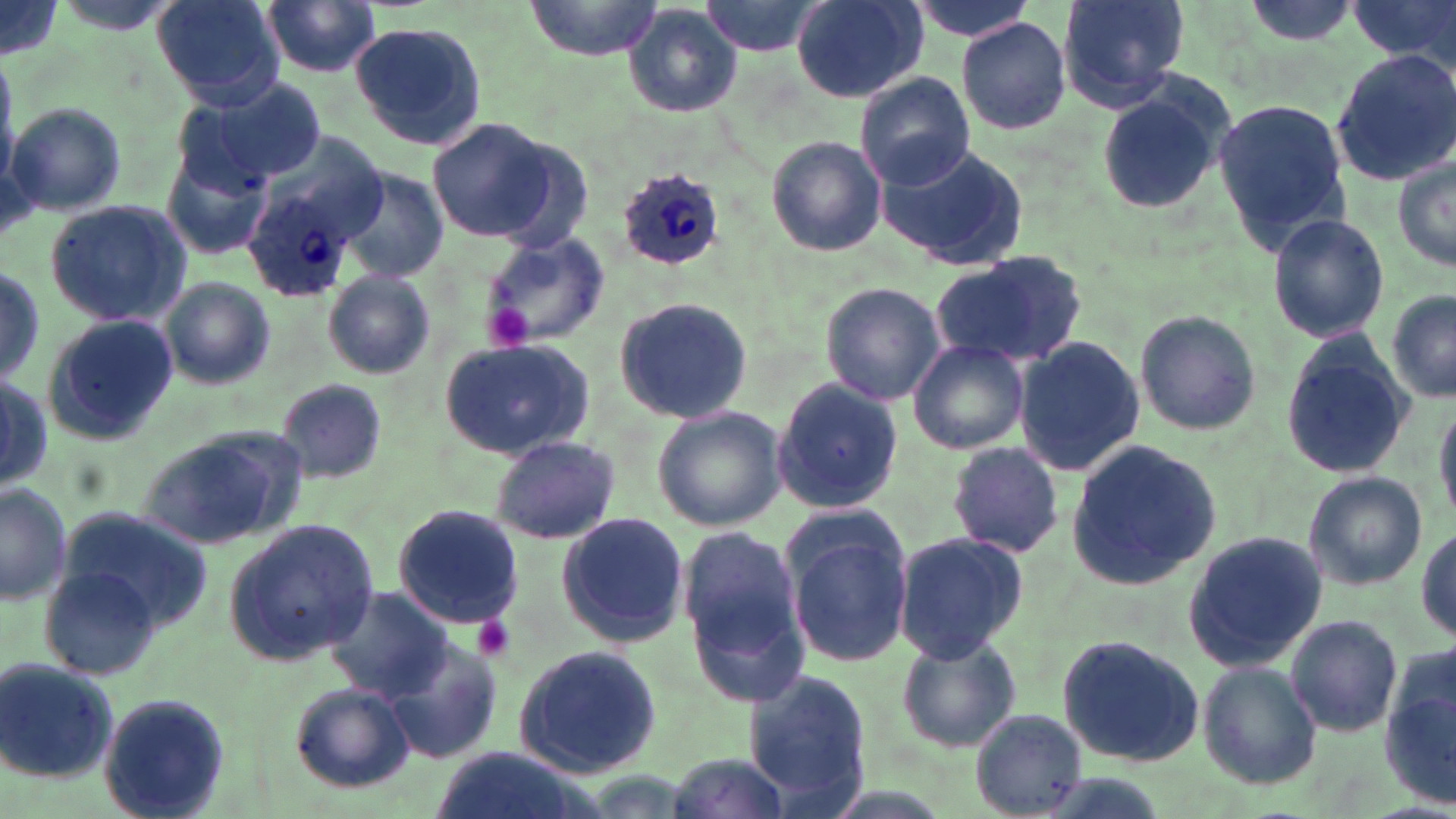

{
  "slide_level_diagnosis": "Plasmodium ovale",
  "magnification": "1000x",
  "stain": "May-Grünwald-Giemsa",
  "field_of_view": "single",
  "preparation": "thin blood smear",
  "modality": "optical microscopy",
  "image_size": "1456×819 pixels",
  "uninfected_red_blood_cell_locations": "approximate bounding boxes as named x1/y1/x2/y2 corners in pixels: (x1=152, y1=0, x2=284, y2=108), (x1=520, y1=0, x2=665, y2=60), (x1=700, y1=0, x2=829, y2=57), (x1=791, y1=0, x2=927, y2=102), (x1=902, y1=0, x2=1039, y2=44), (x1=1057, y1=0, x2=1191, y2=109), (x1=1236, y1=0, x2=1363, y2=48), (x1=1348, y1=0, x2=1456, y2=68), (x1=260, y1=1, x2=381, y2=79), (x1=0, y1=2, x2=61, y2=59), (x1=624, y1=6, x2=741, y2=117), (x1=956, y1=17, x2=1071, y2=134), (x1=349, y1=20, x2=487, y2=150), (x1=1329, y1=49, x2=1456, y2=184), (x1=855, y1=74, x2=977, y2=191), (x1=207, y1=77, x2=329, y2=186), (x1=1095, y1=86, x2=1227, y2=216), (x1=1214, y1=97, x2=1350, y2=255), (x1=8, y1=102, x2=127, y2=218), (x1=429, y1=118, x2=555, y2=241), (x1=486, y1=135, x2=597, y2=250), (x1=766, y1=135, x2=887, y2=256), (x1=877, y1=144, x2=1029, y2=269), (x1=159, y1=146, x2=275, y2=264), (x1=1391, y1=157, x2=1456, y2=274), (x1=336, y1=169, x2=449, y2=281), (x1=42, y1=198, x2=191, y2=326), (x1=1266, y1=212, x2=1389, y2=344), (x1=479, y1=229, x2=612, y2=349), (x1=933, y1=254, x2=1088, y2=369), (x1=0, y1=262, x2=46, y2=390), (x1=321, y1=269, x2=436, y2=379), (x1=159, y1=278, x2=276, y2=390), (x1=819, y1=280, x2=946, y2=405), (x1=1386, y1=290, x2=1456, y2=403), (x1=612, y1=297, x2=756, y2=427), (x1=1132, y1=309, x2=1265, y2=437), (x1=37, y1=315, x2=177, y2=444), (x1=441, y1=335, x2=593, y2=457), (x1=1016, y1=336, x2=1144, y2=475), (x1=1279, y1=336, x2=1418, y2=481), (x1=907, y1=339, x2=1029, y2=455), (x1=0, y1=371, x2=51, y2=494), (x1=769, y1=377, x2=904, y2=514), (x1=273, y1=379, x2=387, y2=484), (x1=1433, y1=397, x2=1455, y2=525), (x1=651, y1=406, x2=783, y2=532), (x1=138, y1=424, x2=304, y2=549), (x1=488, y1=435, x2=622, y2=546), (x1=1066, y1=441, x2=1223, y2=588), (x1=947, y1=442, x2=1062, y2=558), (x1=1304, y1=471, x2=1428, y2=590), (x1=0, y1=482, x2=73, y2=606), (x1=392, y1=504, x2=522, y2=629), (x1=55, y1=508, x2=214, y2=629), (x1=555, y1=512, x2=691, y2=649), (x1=225, y1=516, x2=378, y2=665), (x1=679, y1=521, x2=811, y2=698), (x1=1414, y1=523, x2=1454, y2=646), (x1=785, y1=526, x2=913, y2=668), (x1=891, y1=531, x2=1028, y2=663), (x1=1181, y1=532, x2=1328, y2=670), (x1=42, y1=567, x2=165, y2=681), (x1=326, y1=587, x2=454, y2=700), (x1=1286, y1=614, x2=1403, y2=737), (x1=1054, y1=632, x2=1206, y2=765), (x1=895, y1=633, x2=1023, y2=753), (x1=382, y1=642, x2=505, y2=767), (x1=1383, y1=642, x2=1456, y2=811), (x1=514, y1=645, x2=664, y2=777), (x1=0, y1=655, x2=118, y2=786), (x1=1197, y1=659, x2=1322, y2=790), (x1=741, y1=670, x2=876, y2=815), (x1=290, y1=683, x2=415, y2=794), (x1=99, y1=695, x2=230, y2=819), (x1=973, y1=709, x2=1087, y2=817), (x1=432, y1=749, x2=592, y2=819), (x1=665, y1=751, x2=795, y2=819)",
  "plasmodium_ovale_infected_red_blood_cell_locations": "approximate bounding boxes as named x1/y1/x2/y2 corners in pixels: (x1=617, y1=168, x2=731, y2=271), (x1=242, y1=183, x2=360, y2=301)",
  "platelet_locations": "approximate bounding boxes as named x1/y1/x2/y2 corners in pixels: (x1=483, y1=302, x2=536, y2=350), (x1=472, y1=614, x2=517, y2=662)"
}